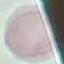
Summary:
  - Result: no malaria parasites seen
  - Preparation: thin smear
  - Capture: smartphone through the microscope eyepiece
  - Stain: Giemsa
  - Image type: cell patch, automatically extracted from a larger field of view and resized to 64 × 64 pixels